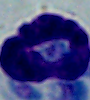

magnification = 1000x
identification = white blood cell
modality = micrograph